Report the malaria status of this cell.
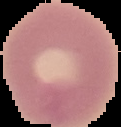

Uninfected.

Cell region segmented out of the field of view; the surrounding area is masked to black. Image is 121×127 pixels. From a thin blood smear.